Identify the parasite.
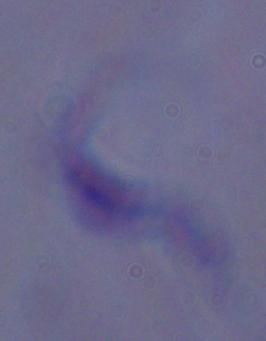

This is a trypanosome.

1000x magnification. Photomicrograph.